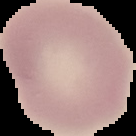

Malaria status: uninfected. Cell region segmented out of the field of view; the surrounding area is masked to black. Image is 136×136 pixels. From a thin blood film.